State which parasite is depicted.
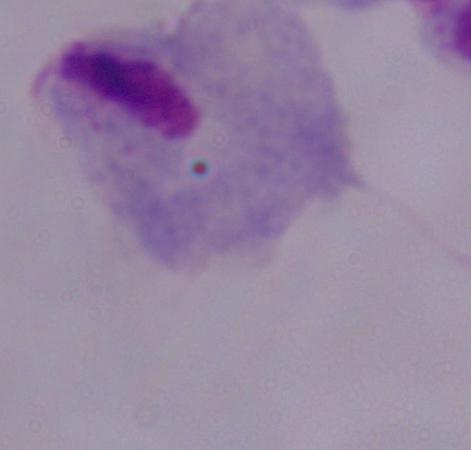
This is a trichomonad.

{
  "modality": "photomicrograph",
  "magnification": "1000x"
}